Outline each uninfected red blood cell.
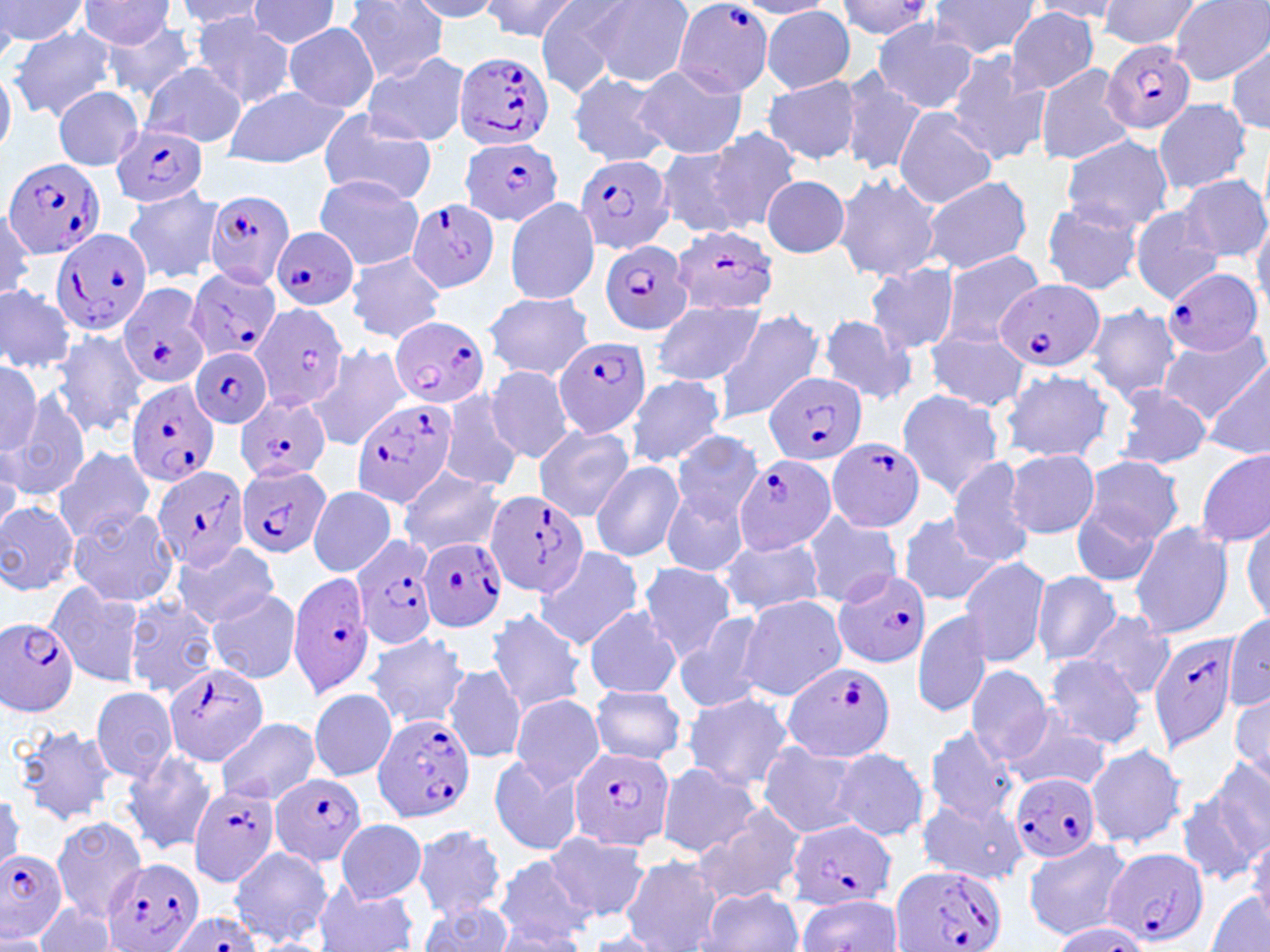

Approximate bounding boxes as (x1, y1, x2, y2) in pixels.
Uninfected red blood cells: (0, 0, 89, 46), (343, 0, 450, 83), (408, 0, 507, 20), (480, 0, 580, 42), (534, 0, 637, 93), (586, 0, 694, 87), (828, 0, 938, 42), (929, 0, 1040, 57), (1098, 0, 1203, 51), (176, 1, 268, 31), (244, 1, 341, 49), (735, 1, 839, 19), (1025, 1, 1126, 20), (1170, 1, 1269, 83), (78, 2, 176, 49), (761, 6, 856, 92), (1005, 8, 1100, 96), (193, 15, 295, 109), (870, 19, 979, 114), (101, 21, 200, 102), (283, 23, 380, 111), (8, 24, 116, 121), (1229, 41, 1268, 131), (362, 51, 471, 148), (945, 51, 1051, 165), (140, 61, 247, 148), (1034, 62, 1138, 166), (632, 64, 746, 160), (0, 66, 15, 159), (838, 69, 927, 178), (566, 72, 672, 167), (762, 74, 861, 164), (52, 86, 143, 169), (227, 86, 349, 167), (1152, 97, 1251, 195), (316, 107, 438, 203), (895, 108, 997, 209), (707, 126, 800, 231), (1060, 134, 1173, 232), (654, 145, 760, 240), (833, 171, 941, 282), (760, 174, 850, 257), (918, 174, 1033, 275), (1177, 174, 1269, 262), (314, 175, 424, 269), (122, 186, 225, 284), (503, 197, 601, 304), (1040, 200, 1145, 296), (0, 209, 37, 298), (1129, 209, 1224, 303), (1250, 213, 1270, 314), (936, 248, 1048, 350), (346, 251, 446, 342), (864, 261, 959, 354), (0, 284, 75, 374), (484, 290, 593, 380), (650, 299, 764, 387), (1084, 305, 1183, 401), (710, 308, 827, 424), (815, 313, 917, 405), (1156, 325, 1269, 423), (52, 327, 149, 437), (928, 331, 1030, 411), (310, 344, 411, 449), (0, 358, 42, 454), (1203, 359, 1269, 456), (485, 365, 575, 464), (998, 366, 1116, 464), (624, 374, 727, 467), (1112, 384, 1213, 470), (894, 389, 1003, 499), (7, 391, 90, 501), (442, 391, 524, 492), (533, 424, 635, 521), (672, 433, 763, 523), (54, 445, 155, 544), (1194, 447, 1270, 549), (1005, 449, 1099, 539), (1081, 454, 1185, 546), (945, 457, 1038, 568), (590, 459, 685, 562), (397, 468, 504, 558), (308, 485, 396, 578), (662, 487, 751, 580), (1071, 498, 1165, 589), (0, 500, 78, 595), (68, 507, 179, 608), (802, 509, 902, 607), (896, 512, 994, 608), (1242, 515, 1270, 623), (1128, 521, 1235, 640), (715, 536, 826, 617), (172, 541, 279, 628), (533, 545, 643, 651), (958, 556, 1050, 667), (638, 563, 739, 661), (1031, 571, 1121, 666), (44, 580, 144, 686), (206, 588, 303, 683), (123, 595, 222, 698), (737, 595, 847, 699), (584, 606, 681, 699), (485, 608, 586, 715), (913, 610, 990, 718), (1080, 611, 1175, 699), (675, 613, 769, 714), (1225, 613, 1270, 711), (365, 631, 472, 729), (1041, 655, 1149, 748), (444, 662, 529, 764), (965, 664, 1052, 766), (91, 685, 179, 781), (588, 685, 686, 765), (307, 688, 398, 782), (680, 692, 795, 791), (510, 694, 605, 788), (1231, 695, 1268, 780), (1000, 706, 1116, 794), (215, 718, 321, 804), (9, 724, 117, 827), (924, 726, 1019, 825), (755, 742, 864, 838), (1085, 742, 1188, 850), (827, 747, 930, 842), (121, 749, 218, 854), (487, 753, 586, 857), (654, 760, 762, 857), (1191, 762, 1269, 876), (917, 797, 1027, 886), (692, 803, 808, 909), (50, 817, 142, 914), (335, 819, 427, 903), (412, 825, 505, 920), (1246, 828, 1270, 923), (547, 831, 650, 923), (1021, 836, 1128, 939), (229, 845, 332, 947), (491, 852, 593, 946), (619, 855, 723, 952), (314, 883, 420, 952), (699, 887, 802, 952), (1204, 893, 1270, 952), (796, 894, 904, 951), (32, 903, 121, 952), (419, 903, 515, 951), (1046, 922, 1152, 952), (487, 927, 585, 951), (585, 931, 664, 951).

Summary:
  - Plasmodium falciparum-infected red blood cell locations: (671, 2, 774, 99), (1102, 41, 1196, 135), (451, 50, 556, 151), (110, 123, 210, 210), (463, 136, 563, 229), (577, 152, 676, 253), (4, 157, 106, 262), (204, 188, 296, 289), (405, 197, 501, 293), (670, 225, 784, 316), (51, 226, 154, 334), (271, 227, 358, 310), (599, 239, 693, 334), (1165, 267, 1264, 358), (186, 268, 282, 363), (993, 279, 1106, 373), (120, 281, 212, 393), (250, 303, 349, 411), (391, 315, 490, 408), (552, 336, 653, 438), (190, 346, 274, 430), (766, 371, 867, 467), (125, 380, 220, 489), (235, 394, 328, 483), (350, 396, 459, 508), (827, 436, 928, 533), (732, 452, 837, 554), (151, 465, 250, 570), (235, 465, 331, 558), (485, 492, 589, 597), (350, 533, 439, 652), (419, 535, 509, 631), (833, 569, 931, 668), (288, 572, 374, 697), (0, 618, 80, 716), (1147, 630, 1240, 752), (780, 660, 894, 761), (162, 663, 267, 766), (371, 713, 477, 823), (568, 747, 674, 851), (1011, 772, 1101, 865), (269, 773, 368, 867), (188, 785, 280, 886), (786, 819, 895, 911), (1103, 847, 1210, 948), (0, 850, 70, 941), (99, 859, 203, 951), (890, 863, 1007, 952), (166, 912, 261, 952)
  - Slide-level diagnosis: Plasmodium falciparum
  - Image size: 1270×952 pixels
  - Preparation: thin blood film
  - Field of view: single
  - Modality: optical microscopy
  - Magnification: 1000x
  - Stain: May-Grünwald-Giemsa